Comment on the morphology of the red blood cells.
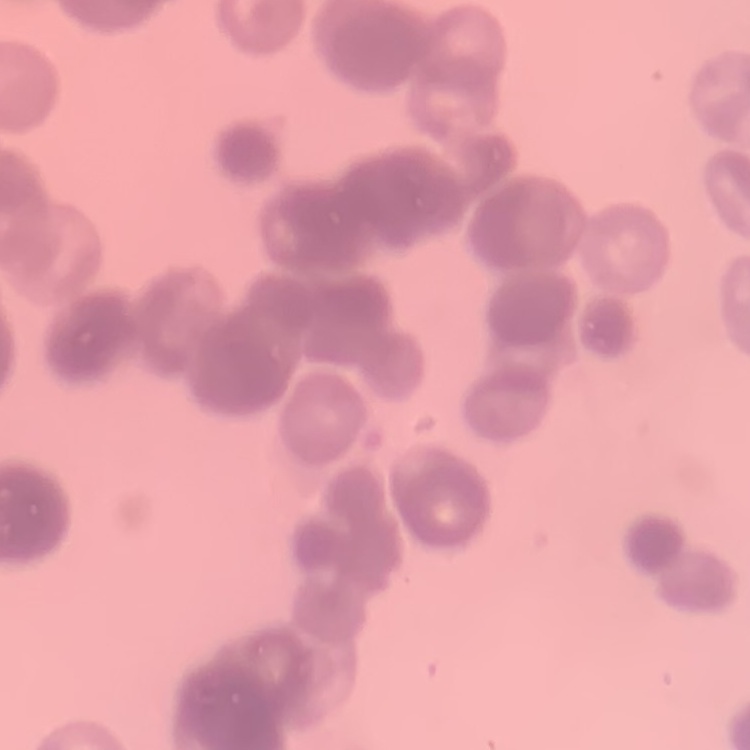

They show rouleaux formation.

Summary:
  - Preparation: thin blood film
  - Stain: Field's or Giemsa
  - Image type: square crop of a larger photomicrograph